Identify the cell.
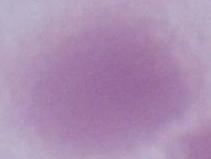

This is an erythrocyte.

modality = photomicrograph
magnification = 1000x